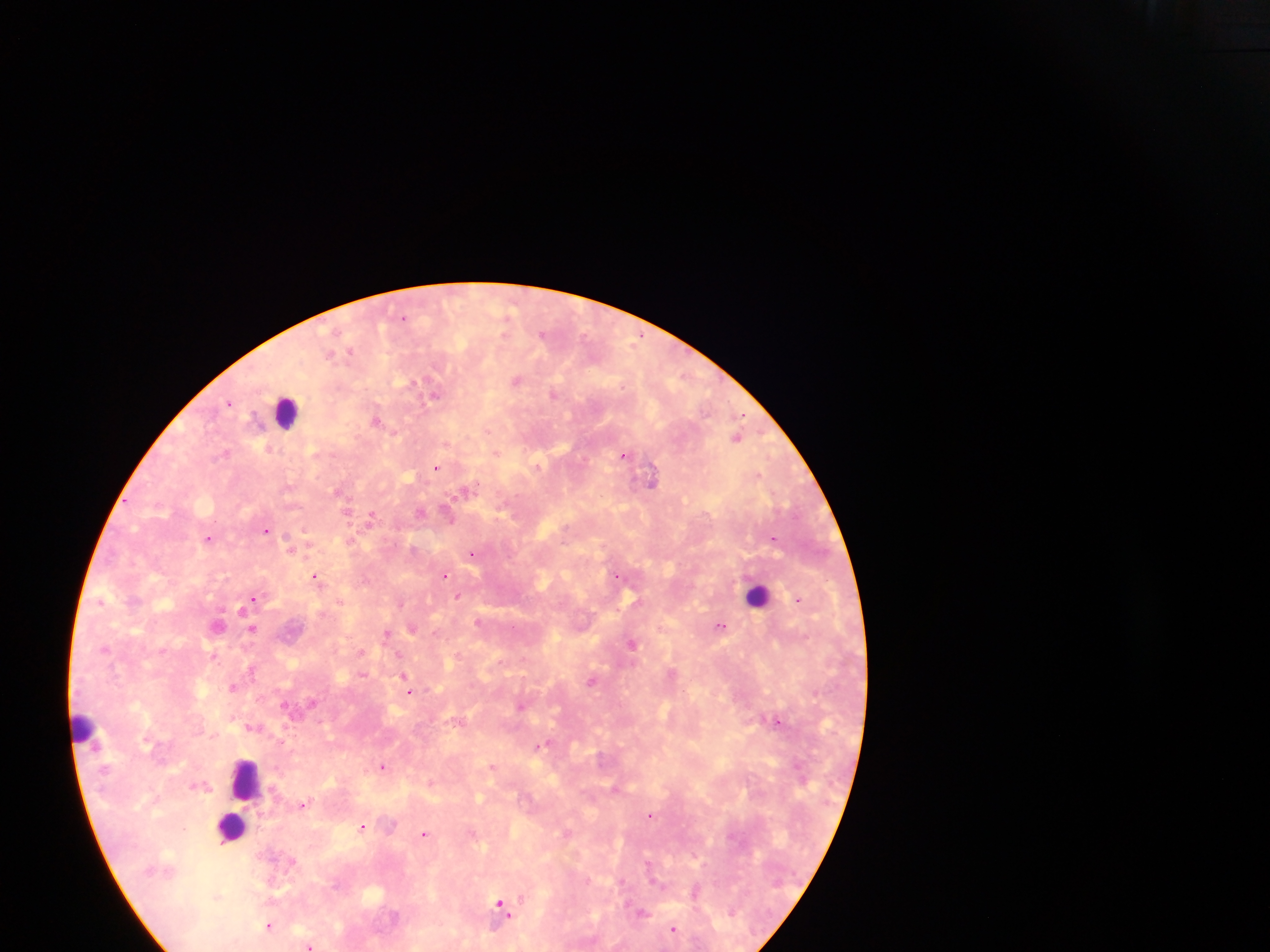 Thick blood film. One field of view. Photographed through a microscope with a mobile-phone camera. Collected in Ghana. Image is 1270×952 pixels.